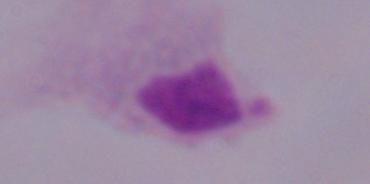

modality = micrograph
magnification = 1000x
identification = trichomonad